Locate every blood parasite and identify its species.
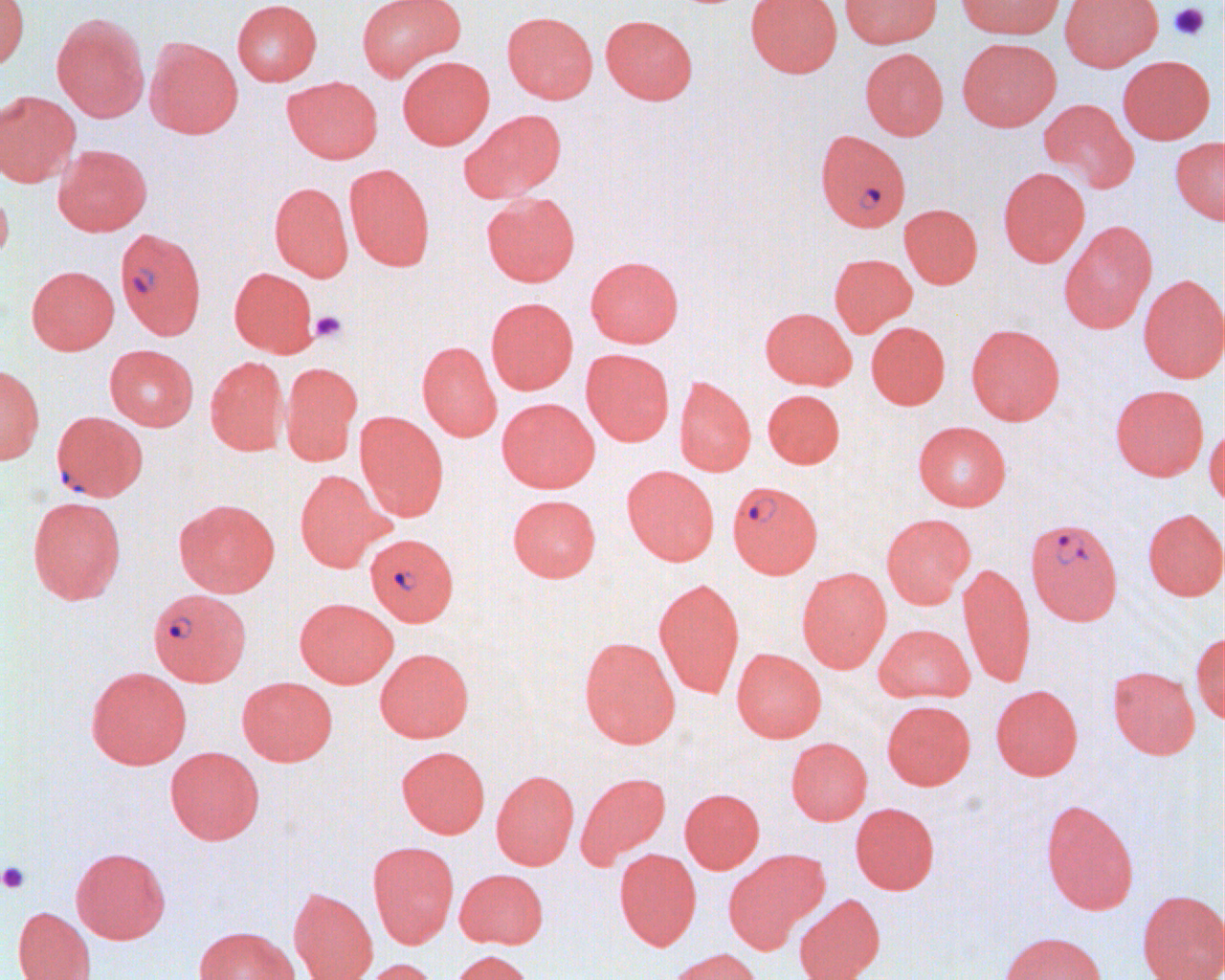
Approximate bounding boxes as (x1,y1)-(x2,y2) corner pairs in pixels.
Plasmodium falciparum-infected red blood cells: (816,129)-(910,232), (115,228)-(206,340), (48,412)-(145,504), (727,480)-(823,578), (1025,516)-(1123,625), (365,533)-(458,626), (148,588)-(251,685).
No Plasmodium ovale, Plasmodium malariae, Plasmodium vivax, Babesia divergens, or Trypanosoma brucei observed.

Platelet locations: (1169,2)-(1210,42), (310,310)-(348,344), (0,861)-(30,893). Uninfected red blood cell locations: (0,0)-(30,70), (232,0)-(322,86), (356,0)-(465,82), (745,0)-(842,77), (839,0)-(942,48), (956,0)-(1064,39), (1059,0)-(1163,71), (502,11)-(598,103), (52,12)-(150,121), (600,14)-(697,105), (145,37)-(243,139), (957,38)-(1061,131), (860,48)-(948,140), (1117,55)-(1214,144), (397,56)-(495,149), (282,76)-(383,164), (0,91)-(80,187), (1038,99)-(1139,194), (461,109)-(567,202), (1170,136)-(1225,226), (53,144)-(152,236), (344,163)-(435,271), (998,166)-(1090,267), (269,182)-(354,281), (0,185)-(14,265), (481,192)-(580,286), (899,204)-(982,289), (1059,221)-(1157,334), (829,253)-(917,337), (585,255)-(684,348), (26,265)-(119,354), (229,267)-(319,357), (1138,274)-(1225,383), (486,297)-(578,394), (759,307)-(857,390), (866,321)-(950,409), (966,323)-(1064,425), (417,341)-(502,441), (104,344)-(199,430), (581,348)-(674,446), (205,356)-(289,456), (281,362)-(362,464), (0,365)-(44,465), (674,376)-(756,476), (1110,384)-(1209,480), (763,389)-(845,468), (497,397)-(599,492), (354,411)-(449,520), (913,420)-(1011,511), (1204,424)-(1225,507), (621,465)-(720,565), (295,469)-(387,572), (508,494)-(601,582), (27,496)-(126,604), (173,498)-(280,597), (1143,508)-(1225,600), (881,512)-(976,608), (958,562)-(1035,687), (796,566)-(891,672), (653,578)-(745,698), (295,597)-(397,688), (874,623)-(974,703), (1191,632)-(1225,724), (579,636)-(680,748), (375,647)-(474,742), (732,648)-(826,742), (1107,665)-(1200,759), (86,666)-(191,769), (236,676)-(338,765), (990,684)-(1082,780), (881,700)-(975,790), (786,736)-(872,825), (397,745)-(490,838), (165,746)-(264,844), (491,770)-(579,869), (576,771)-(671,867), (680,788)-(764,873), (1040,799)-(1139,915), (850,802)-(940,894), (368,841)-(459,948), (70,847)-(170,944), (615,848)-(701,950), (724,850)-(827,952), (454,868)-(548,948), (289,887)-(378,980), (1137,890)-(1224,980), (794,893)-(885,980), (13,906)-(95,980), (194,925)-(300,980), (999,931)-(1107,980), (666,947)-(763,980), (448,949)-(536,980), (356,957)-(440,980). Slide-level diagnosis: Plasmodium falciparum. Light microscopy. Image is 1225×980 pixels. 1000x magnification. One field of a larger specimen. Thin blood smear.